Give the position of every Plasmodium parasite visible.
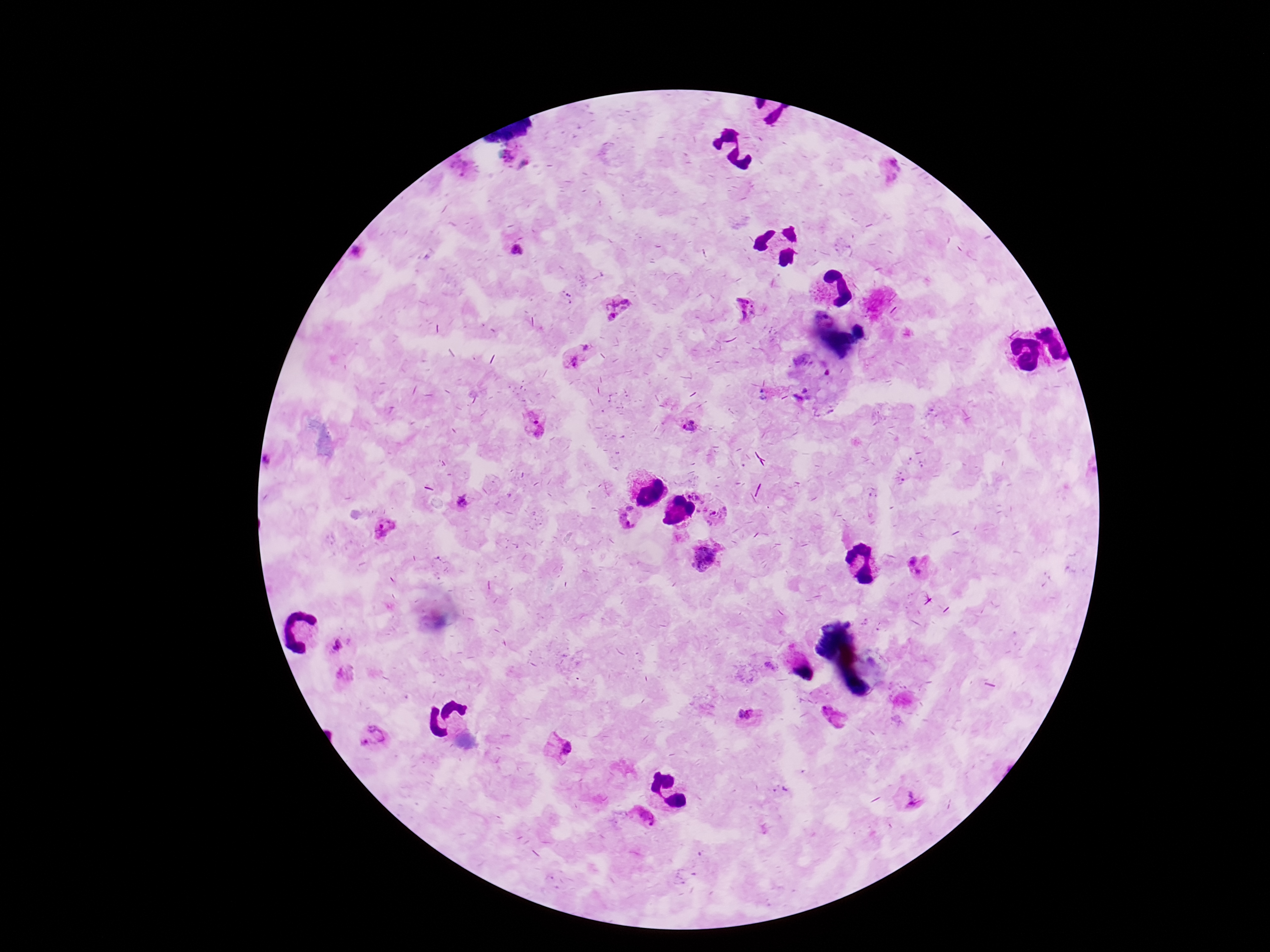
Approximate object centers, in pixels from the top-left corner.
Plasmodium parasites: (x=506, y=156), (x=460, y=164), (x=526, y=164), (x=891, y=168), (x=518, y=251), (x=360, y=253), (x=615, y=306), (x=747, y=308), (x=585, y=348), (x=574, y=362), (x=533, y=423), (x=688, y=424), (x=700, y=493), (x=462, y=502), (x=715, y=514), (x=632, y=518), (x=385, y=530), (x=705, y=556), (x=921, y=565), (x=335, y=645), (x=345, y=674), (x=749, y=714), (x=831, y=716), (x=373, y=740), (x=557, y=747), (x=911, y=801), (x=642, y=819).

patient malaria status = infected
image size = 1270×952 pixels
capture = smartphone camera through the microscope eyepiece
stain = Giemsa
magnification = 100x
field of view = single
preparation = thick blood smear